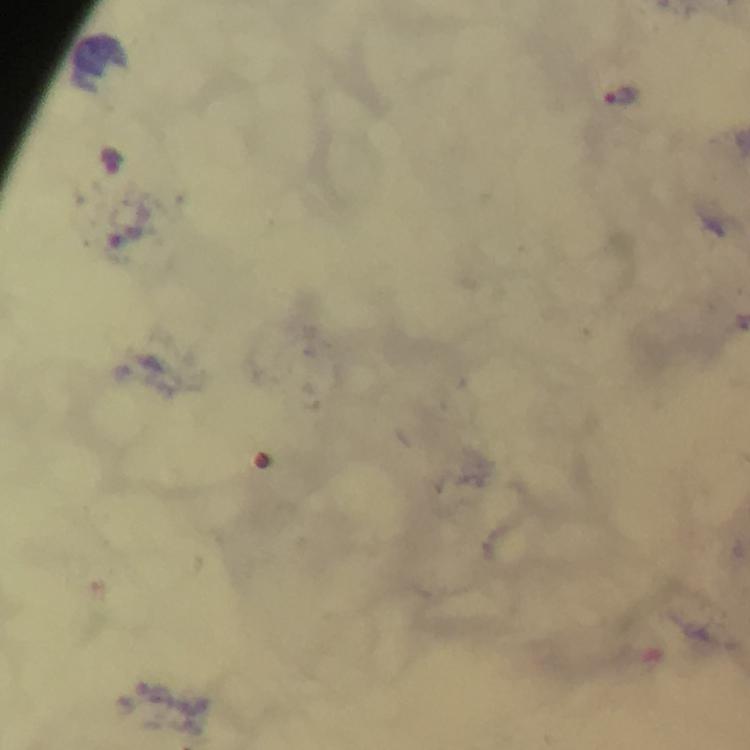

Approximate centers as [x, y] in pixels. Malaria parasite locations: [624, 98], [114, 161]. Image is 750×750 pixels. Photographed through the microscope with a smartphone camera. Immersion oil applied. A crop from one field of view. 100x magnification. From a malaria diagnostic workup. Giemsa-stained preparation. Thick smear.